Comment on the morphology of the red blood cells.
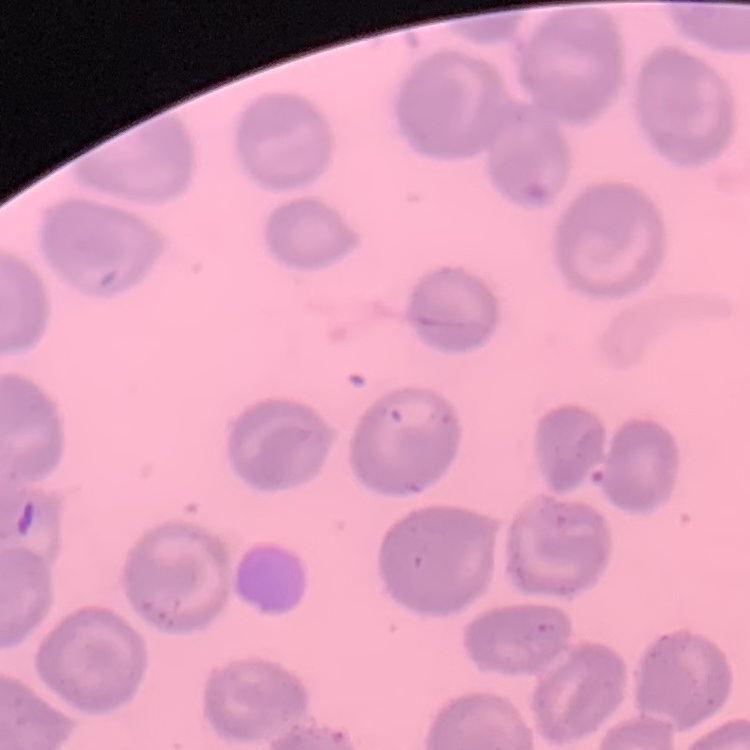
No rouleaux formation.

Square crop of a larger photomicrograph. Field's or Giemsa stain. Thin blood film.